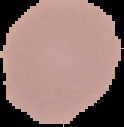
result: no malaria parasites detected
image_type: segmented cell region on a black background
image_size: 124×127 pixels
preparation: thin blood smear